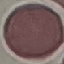
{
  "malaria_status": "uninfected",
  "preparation": "thin blood film",
  "capture": "smartphone through the microscope eyepiece",
  "image_type": "automatically extracted cell patch, resized to 64 × 64 pixels",
  "stain": "Giemsa"
}